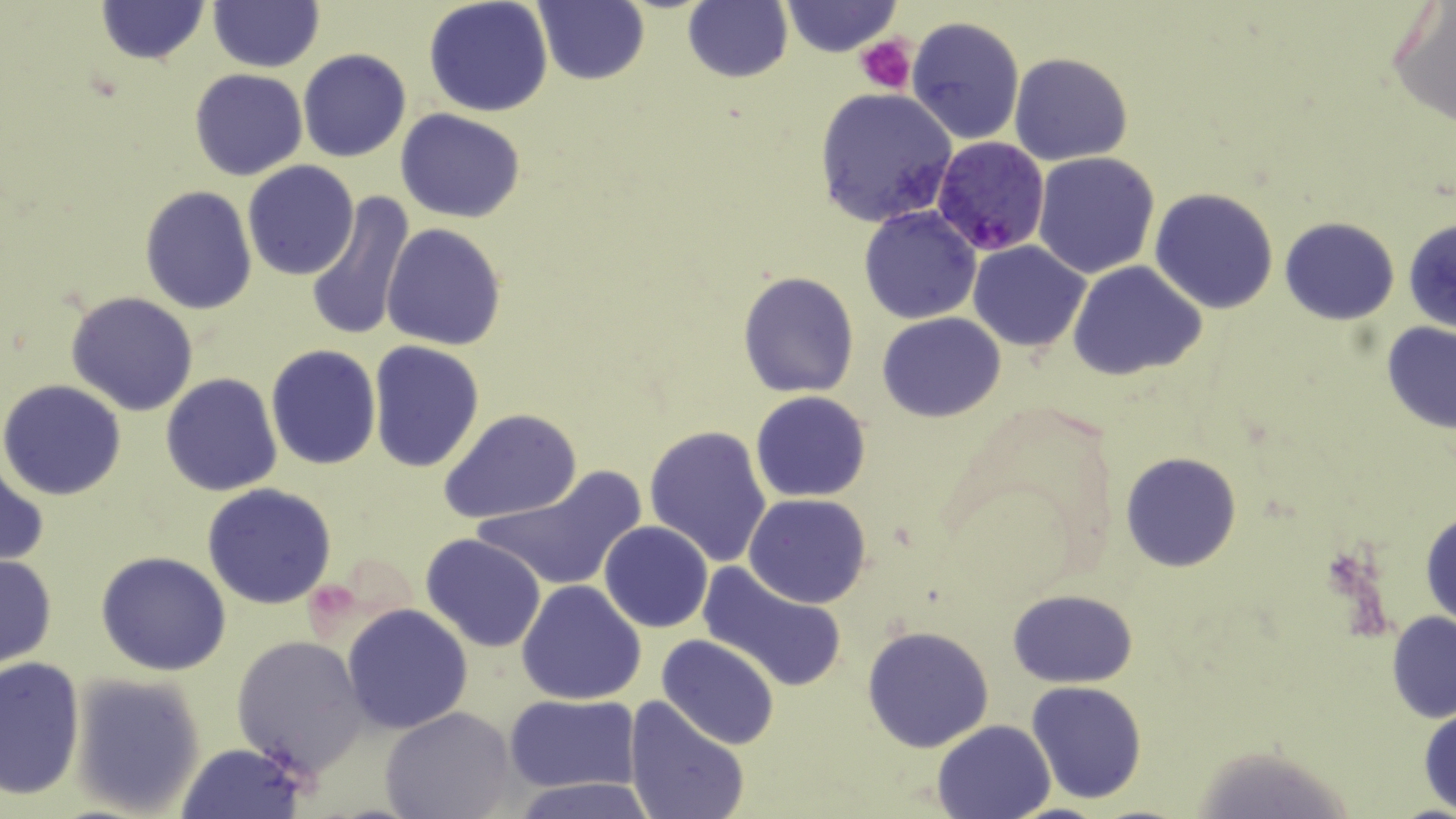
Summary:
  - Coordinate format: approximate bounding boxes as named x1/y1/x2/y2 corners in pixels
  - Uninfected red blood cell locations: (x1=94, y1=0, x2=210, y2=66), (x1=535, y1=0, x2=650, y2=86), (x1=683, y1=0, x2=793, y2=84), (x1=424, y1=1, x2=553, y2=118), (x1=208, y1=2, x2=324, y2=72), (x1=1387, y1=2, x2=1456, y2=130), (x1=781, y1=3, x2=902, y2=55), (x1=907, y1=17, x2=1025, y2=145), (x1=298, y1=48, x2=412, y2=162), (x1=1010, y1=52, x2=1132, y2=166), (x1=189, y1=68, x2=309, y2=181), (x1=813, y1=89, x2=956, y2=228), (x1=395, y1=109, x2=526, y2=223), (x1=1032, y1=152, x2=1162, y2=280), (x1=242, y1=162, x2=356, y2=279), (x1=139, y1=185, x2=257, y2=316), (x1=1150, y1=188, x2=1280, y2=314), (x1=303, y1=190, x2=417, y2=344), (x1=859, y1=206, x2=982, y2=323), (x1=1279, y1=216, x2=1399, y2=324), (x1=1403, y1=217, x2=1456, y2=333), (x1=382, y1=224, x2=507, y2=351), (x1=968, y1=240, x2=1091, y2=351), (x1=1068, y1=261, x2=1207, y2=383), (x1=736, y1=270, x2=859, y2=397), (x1=66, y1=291, x2=199, y2=416), (x1=877, y1=311, x2=1006, y2=423), (x1=1380, y1=322, x2=1456, y2=434), (x1=368, y1=341, x2=485, y2=472), (x1=266, y1=344, x2=380, y2=469), (x1=161, y1=372, x2=282, y2=496), (x1=0, y1=379, x2=128, y2=501), (x1=750, y1=391, x2=872, y2=503), (x1=437, y1=408, x2=581, y2=525), (x1=644, y1=424, x2=772, y2=566), (x1=1120, y1=452, x2=1241, y2=572), (x1=0, y1=464, x2=49, y2=568), (x1=472, y1=465, x2=650, y2=597), (x1=201, y1=484, x2=337, y2=609), (x1=744, y1=493, x2=872, y2=607), (x1=1420, y1=506, x2=1455, y2=631), (x1=600, y1=521, x2=713, y2=633), (x1=420, y1=534, x2=548, y2=654), (x1=96, y1=551, x2=231, y2=677), (x1=0, y1=553, x2=57, y2=667), (x1=698, y1=562, x2=849, y2=692), (x1=516, y1=580, x2=645, y2=705), (x1=1009, y1=589, x2=1138, y2=687), (x1=341, y1=604, x2=473, y2=734), (x1=1387, y1=612, x2=1455, y2=723), (x1=863, y1=624, x2=995, y2=754), (x1=231, y1=634, x2=369, y2=778), (x1=657, y1=635, x2=781, y2=750), (x1=0, y1=655, x2=86, y2=802), (x1=69, y1=674, x2=206, y2=816), (x1=1025, y1=681, x2=1148, y2=805), (x1=505, y1=693, x2=639, y2=791), (x1=622, y1=696, x2=751, y2=819), (x1=380, y1=705, x2=517, y2=819), (x1=1417, y1=705, x2=1456, y2=814), (x1=931, y1=719, x2=1058, y2=818), (x1=175, y1=742, x2=307, y2=819), (x1=508, y1=778, x2=661, y2=817)
  - Plasmodium falciparum-infected red blood cell locations: (x1=931, y1=138, x2=1052, y2=256)
  - Platelet locations: (x1=856, y1=34, x2=916, y2=93)
  - Slide-level diagnosis: Plasmodium falciparum
  - Stain: May-Grünwald-Giemsa
  - Modality: optical microscopy
  - Image size: 1456×819 pixels
  - Magnification: 1000x
  - Preparation: thin blood film
  - Field of view: single